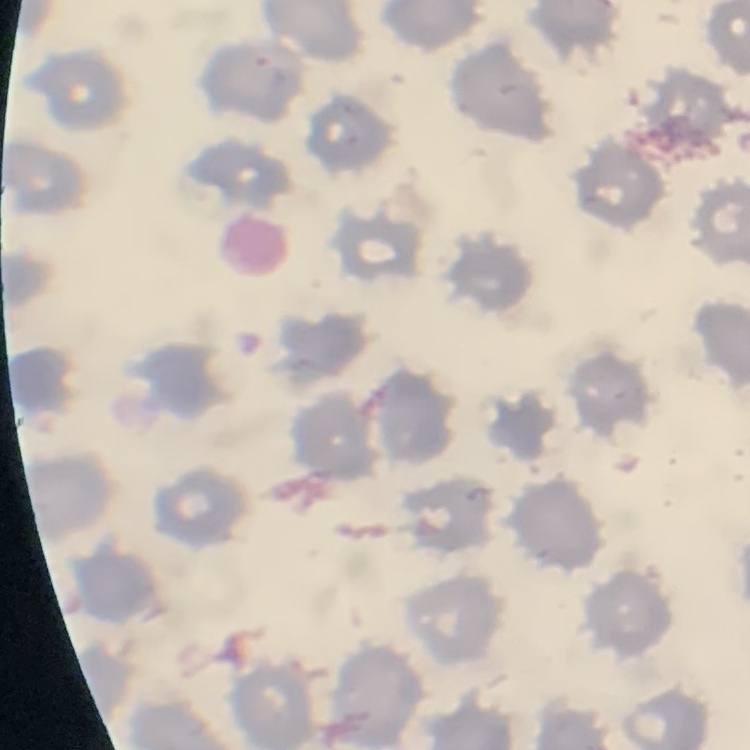

The red blood cells exhibit no rouleaux formation. Thin blood smear. Square crop of a larger photomicrograph. Stained with either Field's or Giemsa.